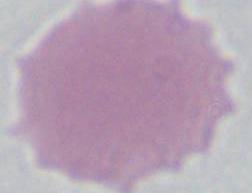 Captured at 1000x magnification. Micrograph. An erythrocyte is shown.